State which parasite is depicted.
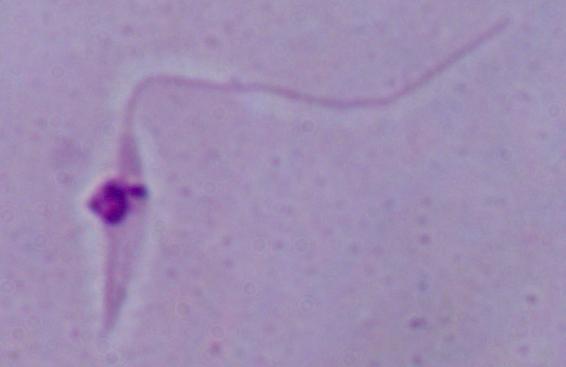

Leishmania.

magnification = 1000x
modality = micrograph